Report the malaria status of this cell.
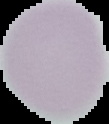
It is uninfected.

Image is 109×124 pixels. From a thin blood film. Segmented cell region on a black background.